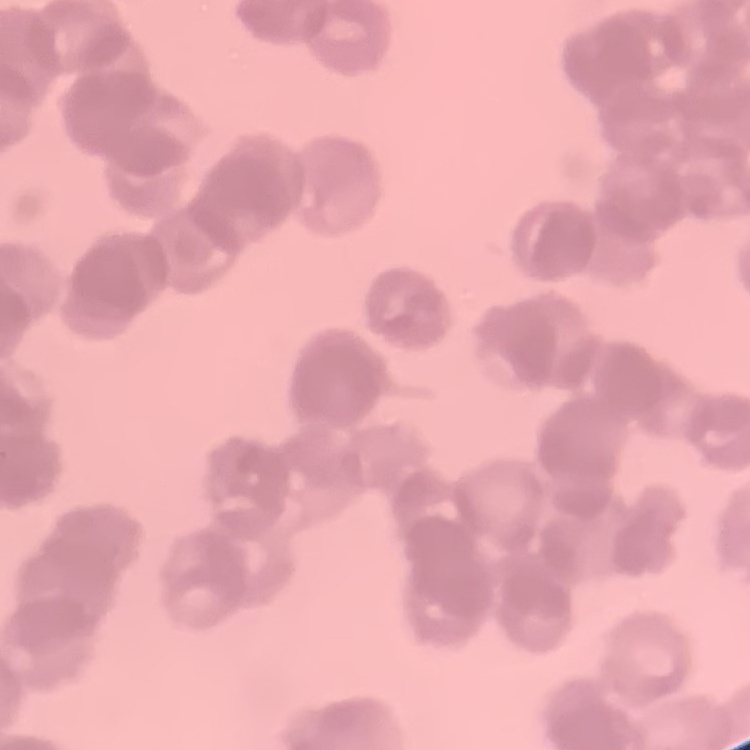

erythrocyte morphology = rouleaux formation
image type = one tile cut from a larger photomicrograph
preparation = thin blood smear
stain = Field's or Giemsa